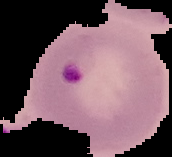 Image is 172×157 pixels. Malaria status: parasitized. From a thin blood film. The area outside the segmented cell region is set to black.